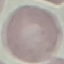

Summary:
  - Malaria status: uninfected
  - Capture: smartphone camera at the microscope eyepiece
  - Stain: Giemsa
  - Preparation: thin blood smear
  - Image type: cell patch, automatically extracted from a larger field of view and resized to 64 × 64 pixels